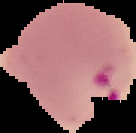

preparation: thin blood smear
result: Plasmodium parasites detected
image_type: segmented cell region on a black background
image_size: 136×133 pixels